Identify the parasite.
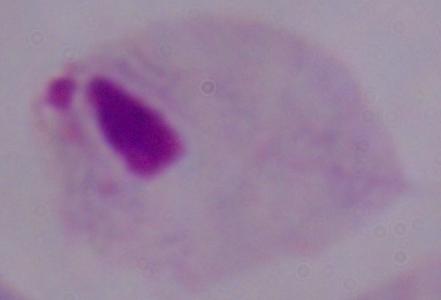

A trichomonad.

1000x magnification. Photomicrograph.